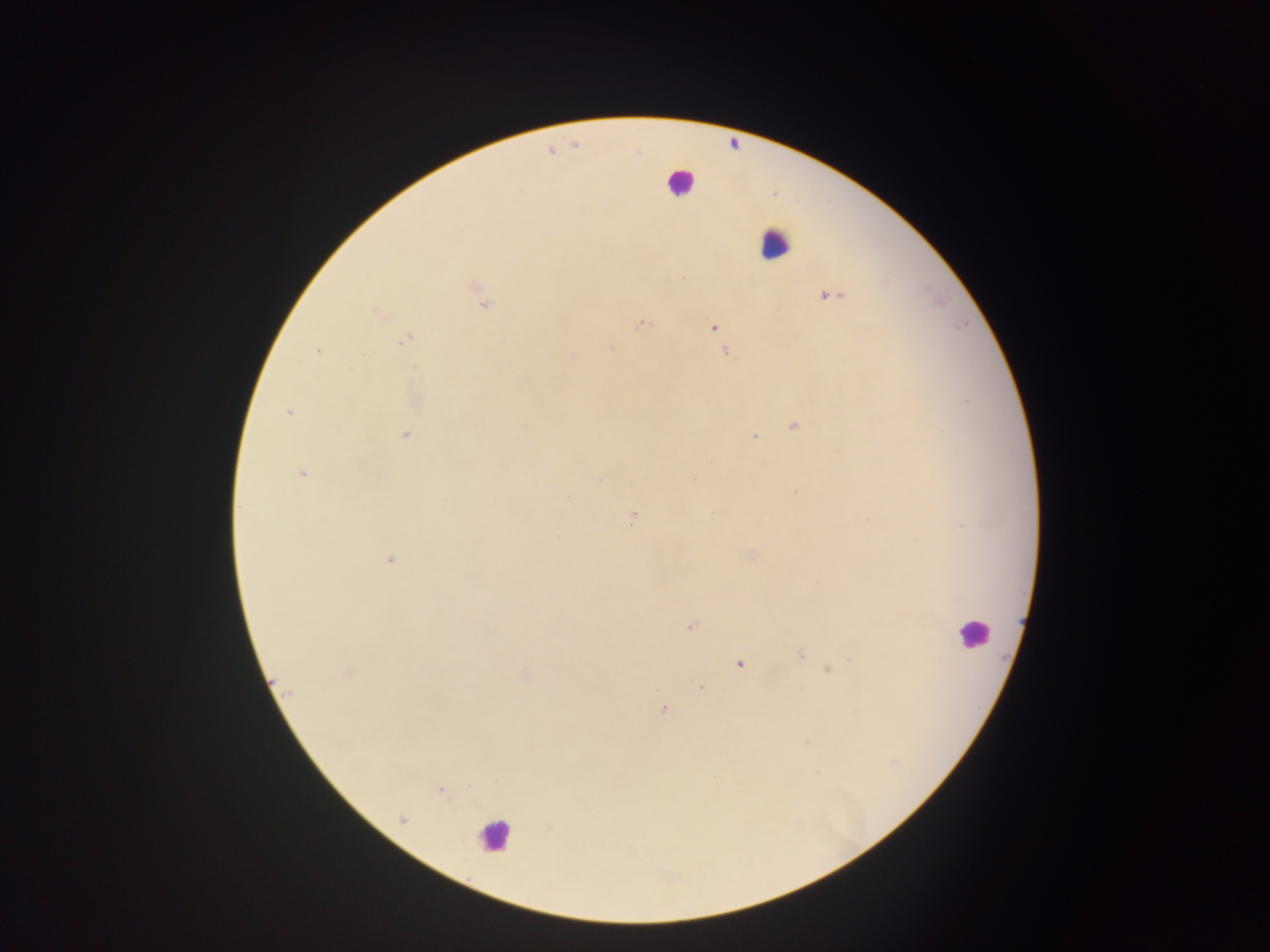
Approximate centers as (x, y) in pixels.
Summary:
  - Plasmodium parasite locations: (682, 278), (477, 289), (829, 296), (483, 303), (378, 313), (641, 324), (713, 326), (404, 339), (611, 349), (318, 350), (727, 352), (572, 356), (288, 412), (793, 427), (405, 435), (754, 437), (302, 474), (796, 492), (632, 517), (556, 537), (390, 560), (690, 627), (800, 655), (740, 664), (828, 670), (348, 674), (700, 688), (663, 709), (440, 791), (549, 829)
  - Leukocyte locations: (734, 141), (680, 182), (775, 243), (972, 632), (493, 836)
  - Field of view: single
  - Preparation: thick blood smear
  - Capture: mobile-phone photograph through a microscope
  - Image size: 1270×952 pixels
  - Country: Ghana